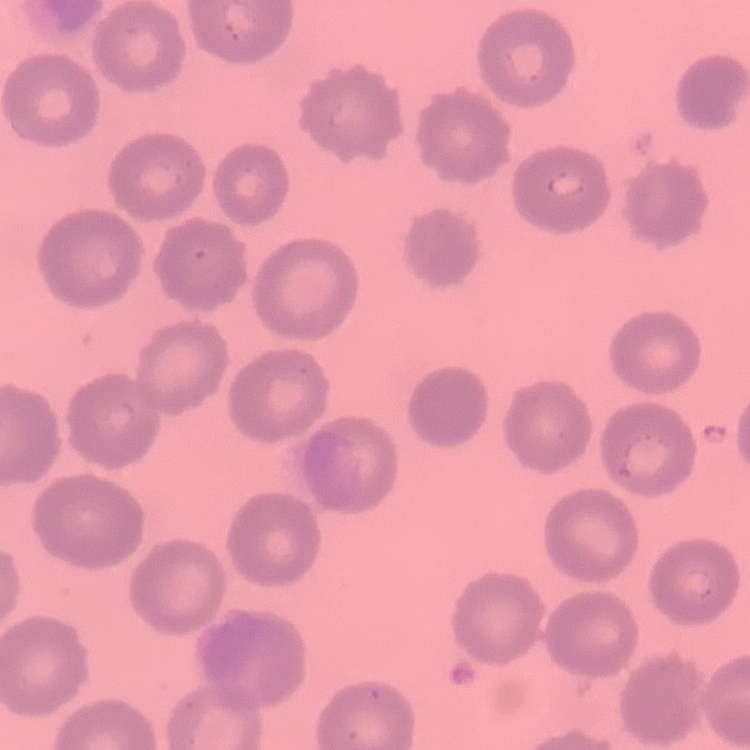 The red blood cells exhibit no rouleaux formation. Field's or Giemsa stain. Square crop of a larger photomicrograph. Thin peripheral smear.